Locate and identify every blood parasite.
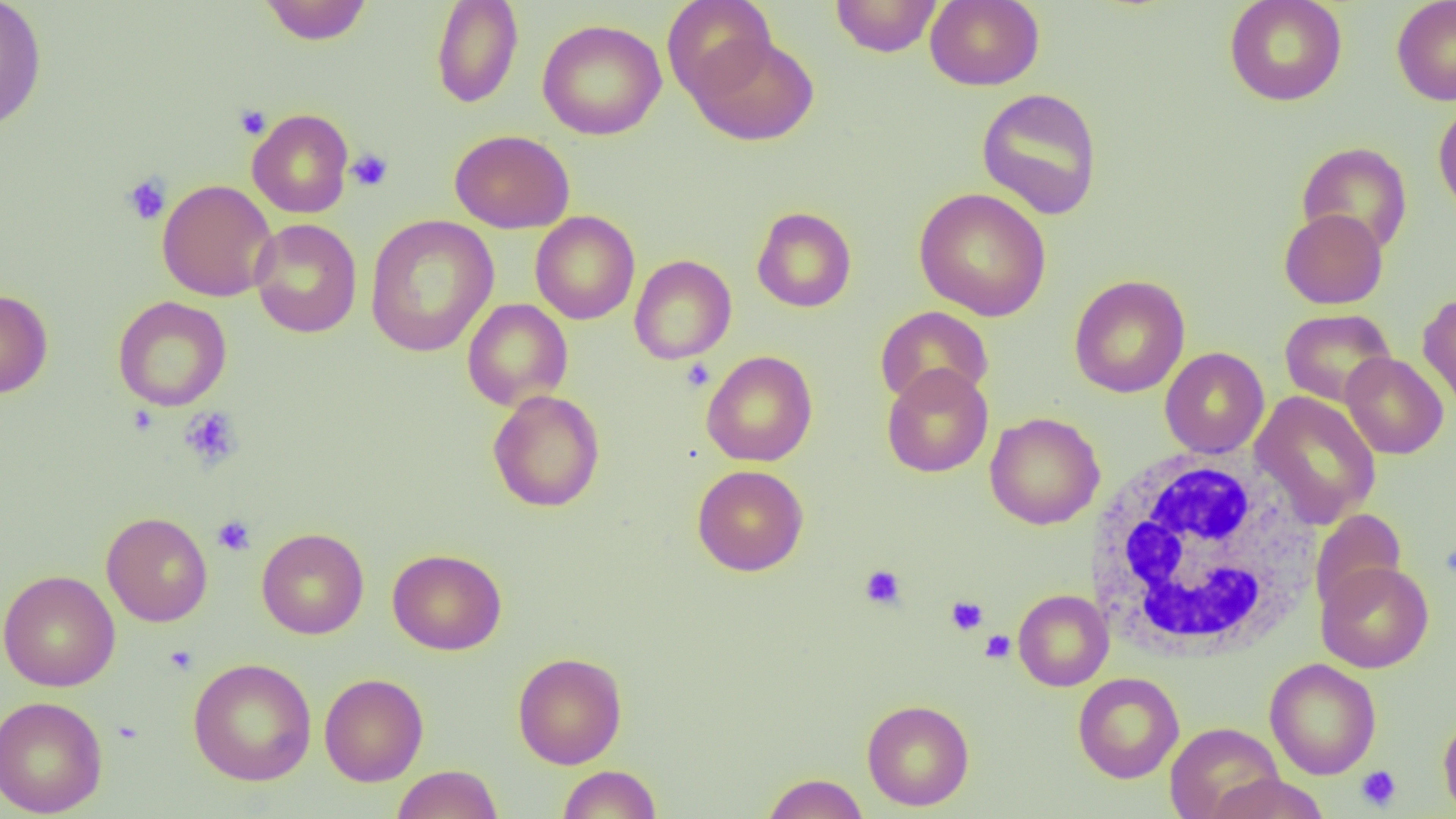

No blood parasites seen.

Approximate bounding boxes as named x1/y1/x2/y2 corners in pixels. Platelet locations: (x1=234, y1=105, x2=271, y2=140), (x1=346, y1=148, x2=393, y2=192), (x1=121, y1=173, x2=172, y2=226), (x1=680, y1=358, x2=715, y2=392), (x1=179, y1=406, x2=243, y2=470), (x1=212, y1=515, x2=256, y2=556), (x1=859, y1=565, x2=906, y2=610), (x1=945, y1=595, x2=988, y2=635), (x1=980, y1=630, x2=1015, y2=663), (x1=164, y1=645, x2=199, y2=675), (x1=1356, y1=765, x2=1401, y2=811). White blood cell locations: (x1=1085, y1=449, x2=1325, y2=662). Uninfected red blood cell locations: (x1=0, y1=0, x2=47, y2=132), (x1=260, y1=0, x2=372, y2=45), (x1=431, y1=0, x2=524, y2=109), (x1=662, y1=0, x2=777, y2=103), (x1=830, y1=0, x2=943, y2=57), (x1=925, y1=0, x2=1045, y2=90), (x1=1223, y1=0, x2=1348, y2=106), (x1=1391, y1=0, x2=1456, y2=106), (x1=537, y1=19, x2=667, y2=141), (x1=689, y1=34, x2=819, y2=146), (x1=976, y1=87, x2=1104, y2=220), (x1=1433, y1=100, x2=1456, y2=217), (x1=246, y1=109, x2=354, y2=218), (x1=449, y1=129, x2=575, y2=233), (x1=1296, y1=141, x2=1413, y2=256), (x1=157, y1=179, x2=277, y2=302), (x1=913, y1=187, x2=1052, y2=321), (x1=752, y1=206, x2=857, y2=312), (x1=1279, y1=208, x2=1388, y2=309), (x1=530, y1=211, x2=640, y2=325), (x1=364, y1=214, x2=499, y2=358), (x1=249, y1=218, x2=362, y2=338), (x1=629, y1=255, x2=737, y2=364), (x1=1068, y1=275, x2=1190, y2=398), (x1=0, y1=289, x2=53, y2=399), (x1=1417, y1=291, x2=1456, y2=414), (x1=112, y1=296, x2=232, y2=412), (x1=462, y1=299, x2=573, y2=411), (x1=875, y1=306, x2=994, y2=408), (x1=1279, y1=308, x2=1396, y2=408), (x1=1160, y1=347, x2=1269, y2=458), (x1=701, y1=350, x2=818, y2=467), (x1=1341, y1=352, x2=1449, y2=459), (x1=881, y1=364, x2=993, y2=478), (x1=487, y1=389, x2=605, y2=512), (x1=1251, y1=390, x2=1381, y2=529), (x1=985, y1=412, x2=1105, y2=530), (x1=692, y1=464, x2=808, y2=576), (x1=1309, y1=509, x2=1407, y2=614), (x1=101, y1=511, x2=213, y2=627), (x1=257, y1=527, x2=369, y2=639), (x1=387, y1=548, x2=507, y2=655), (x1=1316, y1=561, x2=1433, y2=673), (x1=0, y1=569, x2=120, y2=691), (x1=1013, y1=589, x2=1114, y2=691), (x1=512, y1=652, x2=627, y2=769), (x1=188, y1=657, x2=316, y2=786), (x1=1264, y1=658, x2=1381, y2=780), (x1=319, y1=672, x2=429, y2=786), (x1=1072, y1=672, x2=1184, y2=783), (x1=0, y1=695, x2=108, y2=817), (x1=862, y1=700, x2=974, y2=811), (x1=1438, y1=713, x2=1456, y2=818), (x1=1165, y1=722, x2=1284, y2=819), (x1=391, y1=764, x2=503, y2=819), (x1=557, y1=765, x2=662, y2=818), (x1=762, y1=772, x2=869, y2=819), (x1=1205, y1=773, x2=1329, y2=819). Slide-level diagnosis: no evidence of blood parasites. Single field of view. 1000x magnification. Image is 1456×819 pixels. Thin blood film. Light microscopy.